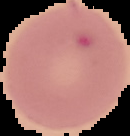

Malaria status: uninfected. Image is 130×136 pixels. Cell region segmented out of the field of view; the surrounding area is masked to black. From a thin blood smear.